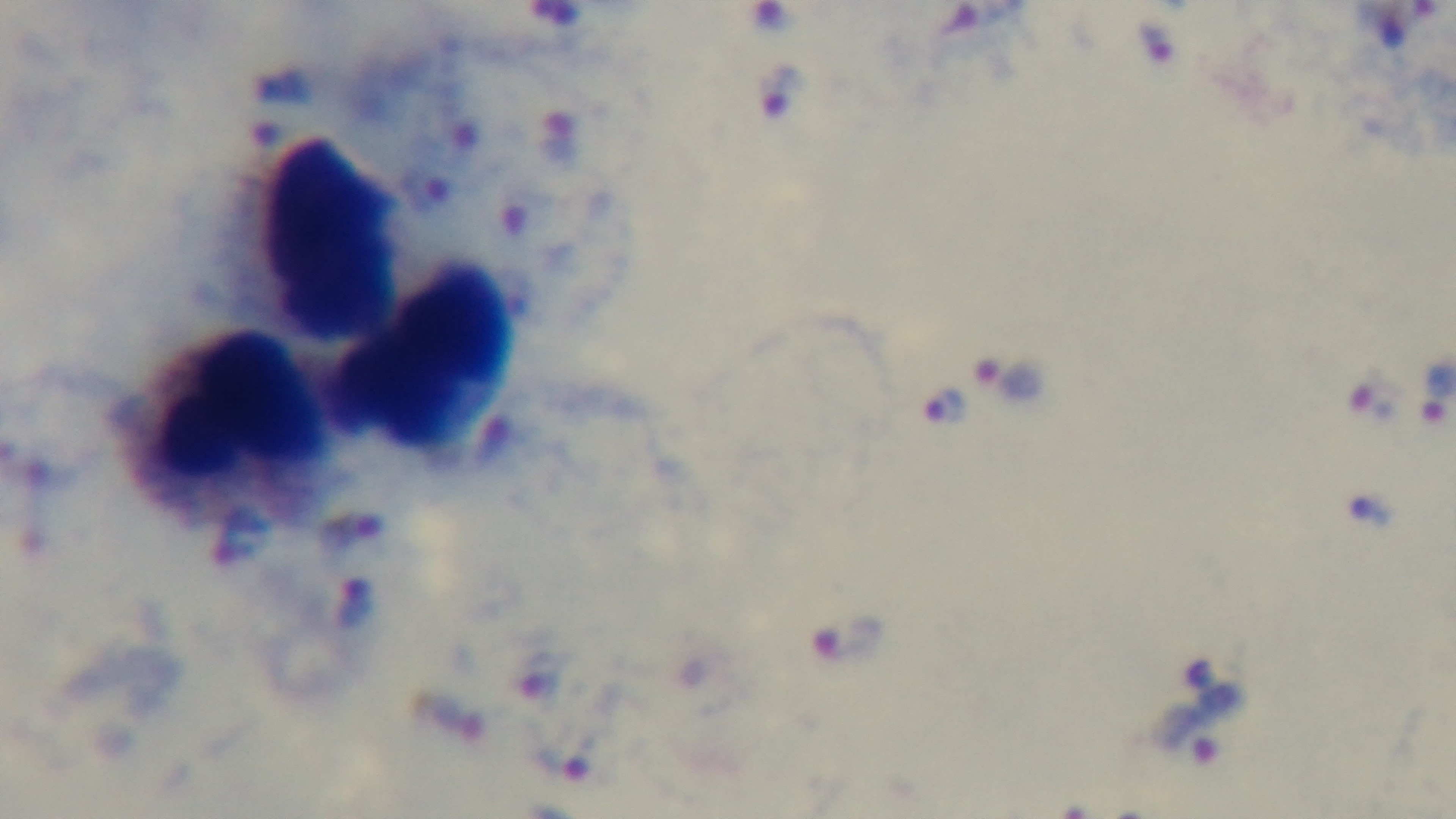
Summary:
  - Capture: mounted 4K digital camera
  - Objective: 100x oil immersion
  - Preparation: thick
  - Stain: Giemsa
  - Modality: light microscopy
  - Malaria status: positive
  - Field of view: one from the slide